State which parasite is depicted.
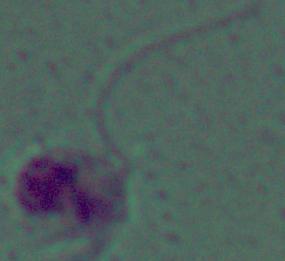
This is Leishmania.

magnification = 1000x
modality = photomicrograph